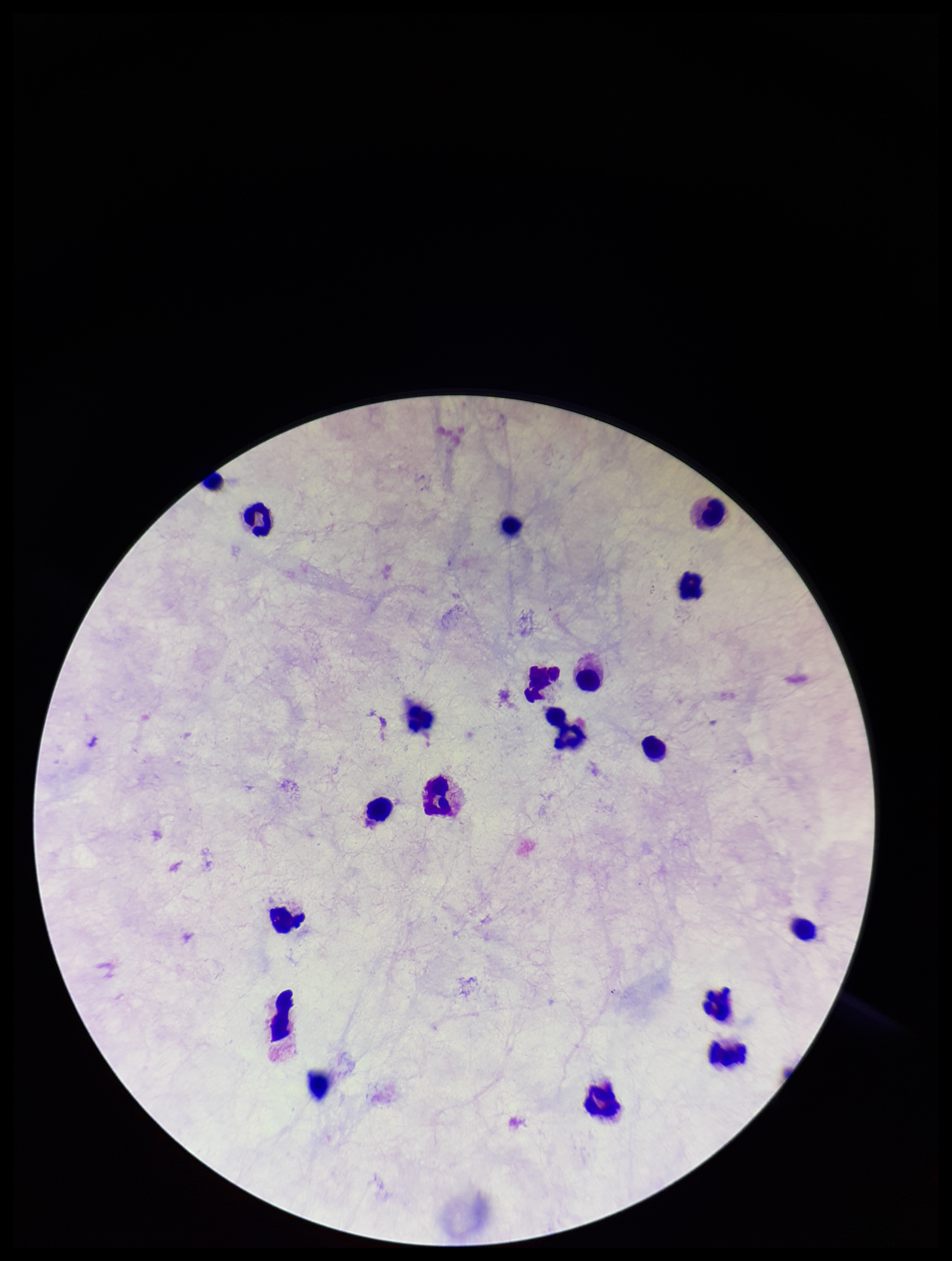 Image is 952×1261 pixels. Parasite count: 0. Smartphone photograph taken through the eyepiece of a microscope. Preparation: thick smear. Plasmodium parasites: none detected. Patient malaria status: negative. Leukocyte count: 18. Giemsa stain. Single field of view.